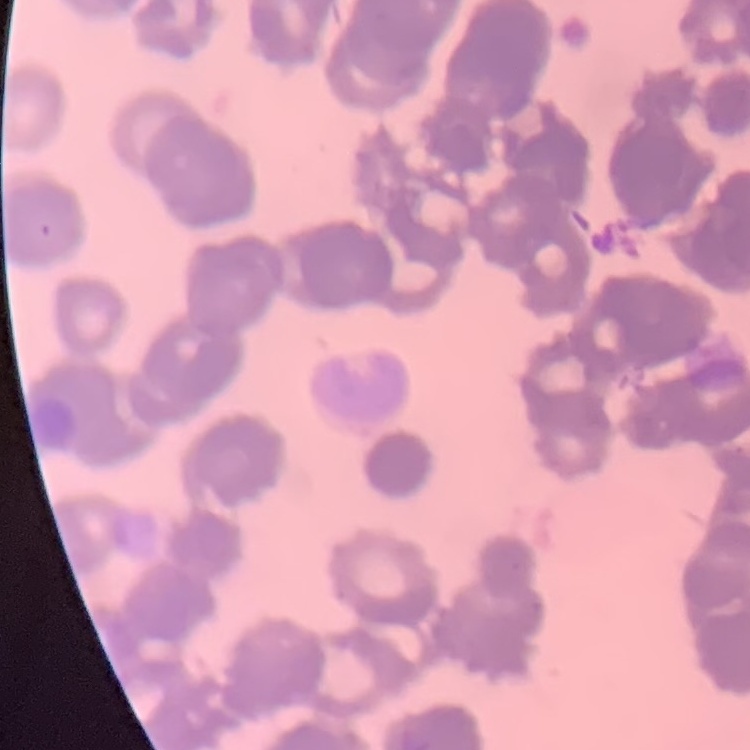
red blood cell morphology = rouleaux formation
image type = one tile cut from a larger photomicrograph
preparation = thin blood film
stain = Field's or Giemsa